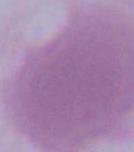
magnification: 1000x
modality: photomicrograph
identification: red blood cell